Classify this cell by malaria status.
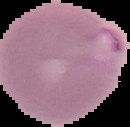

Parasitized.

The area outside the segmented cell region is set to black. Image is 130×127 pixels. From a thin blood smear.